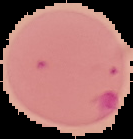
image_size: 133×139 pixels
preparation: thin blood film
result: Plasmodium parasites identified
image_type: segmented cell region with the area outside set to black